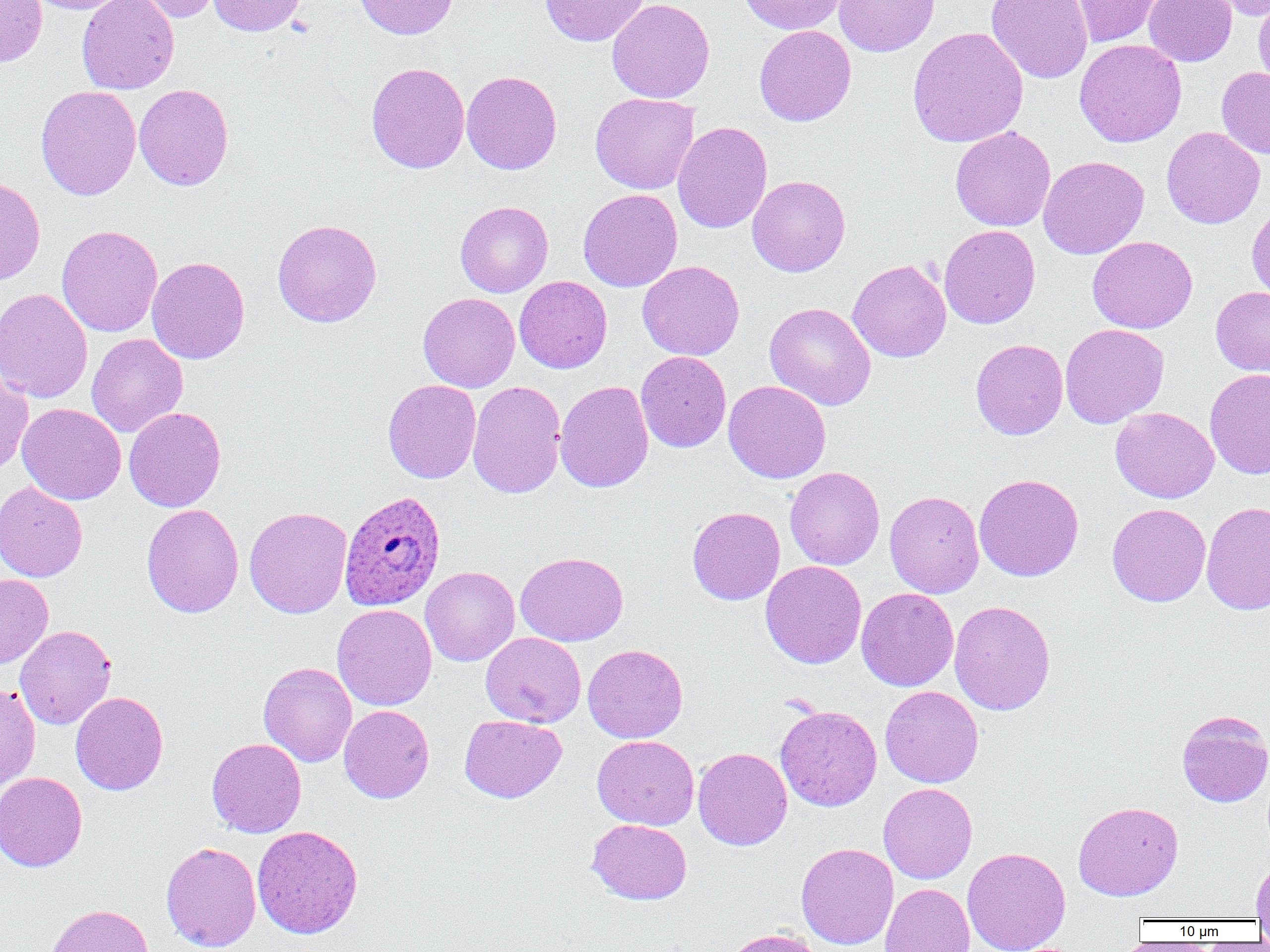
Approximate bounding boxes as named x1/y1/x2/y2 corners in pixels. Uninfected red blood cell locations: (x1=21, y1=0, x2=132, y2=14), (x1=76, y1=0, x2=179, y2=94), (x1=127, y1=0, x2=223, y2=24), (x1=208, y1=0, x2=307, y2=36), (x1=353, y1=0, x2=459, y2=40), (x1=540, y1=0, x2=648, y2=46), (x1=607, y1=0, x2=715, y2=103), (x1=738, y1=0, x2=848, y2=35), (x1=834, y1=0, x2=939, y2=57), (x1=986, y1=0, x2=1093, y2=84), (x1=1068, y1=0, x2=1167, y2=48), (x1=1143, y1=0, x2=1237, y2=66), (x1=1204, y1=0, x2=1270, y2=20), (x1=1253, y1=0, x2=1270, y2=94), (x1=0, y1=1, x2=47, y2=67), (x1=754, y1=25, x2=856, y2=126), (x1=907, y1=26, x2=1029, y2=148), (x1=1074, y1=39, x2=1187, y2=148), (x1=366, y1=61, x2=470, y2=174), (x1=1217, y1=66, x2=1270, y2=159), (x1=462, y1=70, x2=562, y2=175), (x1=134, y1=83, x2=234, y2=190), (x1=36, y1=85, x2=141, y2=200), (x1=590, y1=93, x2=699, y2=193), (x1=672, y1=120, x2=772, y2=234), (x1=950, y1=126, x2=1056, y2=231), (x1=1161, y1=126, x2=1265, y2=229), (x1=1038, y1=155, x2=1150, y2=259), (x1=747, y1=175, x2=850, y2=277), (x1=0, y1=177, x2=45, y2=286), (x1=578, y1=188, x2=682, y2=292), (x1=455, y1=200, x2=553, y2=297), (x1=1247, y1=204, x2=1270, y2=305), (x1=272, y1=218, x2=382, y2=327), (x1=56, y1=225, x2=162, y2=337), (x1=939, y1=225, x2=1041, y2=329), (x1=1087, y1=236, x2=1198, y2=333), (x1=147, y1=256, x2=250, y2=364), (x1=638, y1=260, x2=744, y2=360), (x1=847, y1=260, x2=951, y2=362), (x1=514, y1=276, x2=612, y2=373), (x1=1210, y1=286, x2=1270, y2=376), (x1=0, y1=288, x2=92, y2=403), (x1=418, y1=292, x2=520, y2=392), (x1=764, y1=302, x2=876, y2=410), (x1=1059, y1=323, x2=1169, y2=428), (x1=87, y1=333, x2=187, y2=438), (x1=970, y1=338, x2=1068, y2=440), (x1=636, y1=351, x2=731, y2=453), (x1=0, y1=367, x2=34, y2=476), (x1=1205, y1=369, x2=1270, y2=479), (x1=383, y1=379, x2=481, y2=483), (x1=467, y1=380, x2=566, y2=499), (x1=555, y1=380, x2=654, y2=493), (x1=723, y1=380, x2=831, y2=483), (x1=17, y1=403, x2=126, y2=505), (x1=124, y1=407, x2=226, y2=512), (x1=1110, y1=407, x2=1219, y2=503), (x1=784, y1=466, x2=885, y2=570), (x1=974, y1=473, x2=1084, y2=581), (x1=0, y1=480, x2=88, y2=582), (x1=884, y1=490, x2=984, y2=598), (x1=1201, y1=500, x2=1270, y2=616), (x1=1107, y1=503, x2=1211, y2=606), (x1=141, y1=504, x2=244, y2=618), (x1=244, y1=506, x2=352, y2=619), (x1=687, y1=506, x2=785, y2=605), (x1=515, y1=551, x2=628, y2=646), (x1=760, y1=560, x2=866, y2=669), (x1=420, y1=566, x2=519, y2=666), (x1=0, y1=573, x2=53, y2=668), (x1=856, y1=587, x2=959, y2=691), (x1=949, y1=600, x2=1056, y2=715), (x1=331, y1=604, x2=436, y2=711), (x1=15, y1=625, x2=116, y2=729), (x1=481, y1=632, x2=586, y2=727), (x1=583, y1=643, x2=688, y2=743), (x1=258, y1=662, x2=357, y2=766), (x1=0, y1=680, x2=41, y2=790), (x1=880, y1=685, x2=983, y2=788), (x1=70, y1=691, x2=168, y2=795), (x1=338, y1=704, x2=435, y2=803), (x1=775, y1=705, x2=882, y2=812), (x1=1176, y1=709, x2=1270, y2=807), (x1=459, y1=714, x2=566, y2=802), (x1=592, y1=735, x2=699, y2=830), (x1=206, y1=737, x2=306, y2=838), (x1=693, y1=747, x2=792, y2=851), (x1=0, y1=771, x2=88, y2=872), (x1=878, y1=782, x2=977, y2=884), (x1=1073, y1=801, x2=1183, y2=901), (x1=587, y1=818, x2=692, y2=904), (x1=252, y1=825, x2=364, y2=939), (x1=160, y1=841, x2=261, y2=952), (x1=796, y1=842, x2=899, y2=950), (x1=962, y1=847, x2=1071, y2=952), (x1=1251, y1=859, x2=1270, y2=921), (x1=880, y1=883, x2=975, y2=952), (x1=45, y1=903, x2=154, y2=952), (x1=722, y1=927, x2=826, y2=952). Plasmodium ovale-infected red blood cell locations: (x1=339, y1=490, x2=446, y2=610). Slide-level diagnosis: Plasmodium ovale. Thin blood smear. Light microscopy. One field of a larger specimen. Captured at 1000x magnification. Image is 1270×952 pixels.